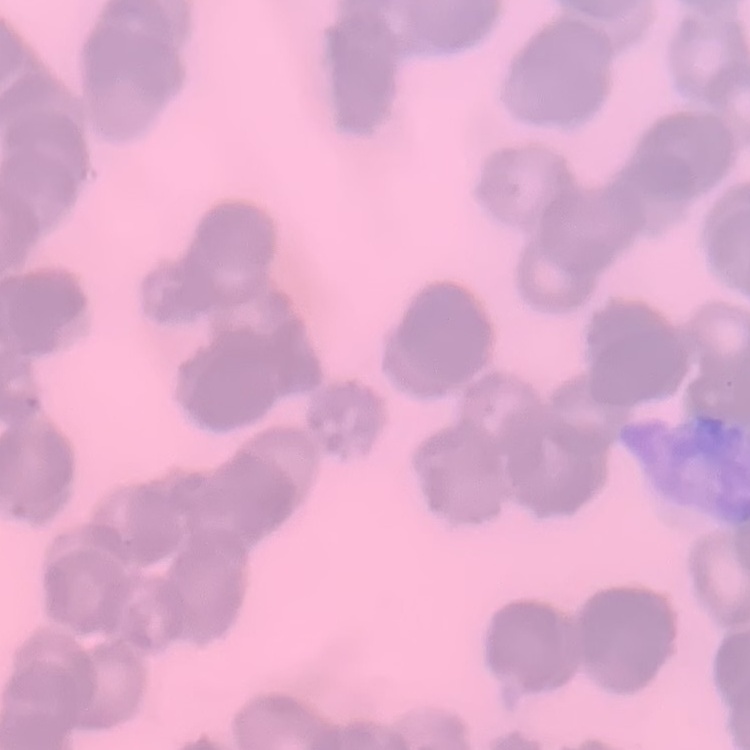
erythrocyte morphology = rouleaux formation
stain = Field's or Giemsa
preparation = thin peripheral smear
image type = square crop of a larger photomicrograph